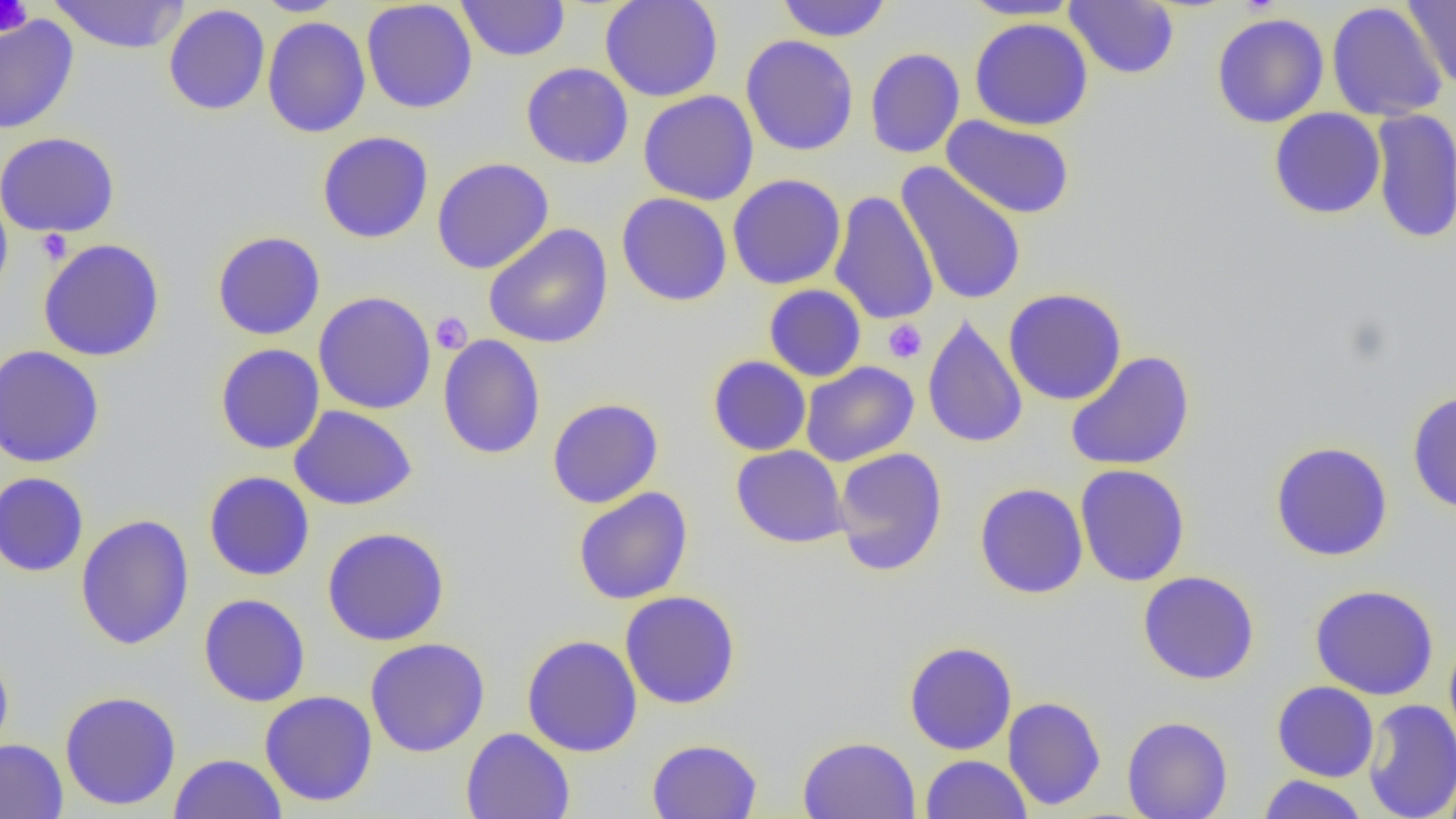

Summary:
  - Coordinate format: approximate bounding boxes as named x1/y1/x2/y2 corners in pixels
  - Uninfected red blood cell locations: (x1=48, y1=0, x2=190, y2=54), (x1=253, y1=0, x2=350, y2=16), (x1=361, y1=0, x2=478, y2=114), (x1=456, y1=0, x2=570, y2=62), (x1=599, y1=0, x2=724, y2=102), (x1=776, y1=0, x2=892, y2=42), (x1=961, y1=0, x2=1084, y2=20), (x1=1403, y1=0, x2=1456, y2=89), (x1=1065, y1=1, x2=1179, y2=79), (x1=1326, y1=2, x2=1448, y2=121), (x1=163, y1=4, x2=271, y2=116), (x1=1212, y1=12, x2=1329, y2=128), (x1=0, y1=15, x2=79, y2=135), (x1=261, y1=16, x2=371, y2=138), (x1=969, y1=17, x2=1094, y2=131), (x1=740, y1=34, x2=859, y2=156), (x1=865, y1=47, x2=965, y2=159), (x1=521, y1=62, x2=634, y2=169), (x1=638, y1=90, x2=759, y2=206), (x1=1268, y1=107, x2=1385, y2=219), (x1=1370, y1=109, x2=1456, y2=244), (x1=941, y1=115, x2=1075, y2=219), (x1=0, y1=131, x2=120, y2=238), (x1=317, y1=131, x2=434, y2=244), (x1=432, y1=157, x2=554, y2=274), (x1=896, y1=161, x2=1028, y2=305), (x1=727, y1=174, x2=846, y2=290), (x1=0, y1=186, x2=13, y2=303), (x1=829, y1=190, x2=939, y2=325), (x1=616, y1=192, x2=733, y2=306), (x1=484, y1=223, x2=613, y2=349), (x1=211, y1=231, x2=326, y2=340), (x1=38, y1=238, x2=165, y2=362), (x1=764, y1=284, x2=866, y2=382), (x1=1003, y1=288, x2=1127, y2=406), (x1=313, y1=291, x2=437, y2=414), (x1=922, y1=314, x2=1028, y2=449), (x1=437, y1=334, x2=546, y2=459), (x1=215, y1=343, x2=325, y2=455), (x1=0, y1=345, x2=105, y2=468), (x1=1064, y1=350, x2=1196, y2=471), (x1=707, y1=355, x2=811, y2=456), (x1=800, y1=361, x2=918, y2=466), (x1=1406, y1=389, x2=1456, y2=514), (x1=547, y1=397, x2=663, y2=508), (x1=289, y1=405, x2=418, y2=510), (x1=1269, y1=441, x2=1393, y2=561), (x1=731, y1=445, x2=848, y2=548), (x1=833, y1=447, x2=948, y2=576), (x1=1075, y1=464, x2=1190, y2=587), (x1=203, y1=471, x2=315, y2=581), (x1=0, y1=472, x2=89, y2=577), (x1=974, y1=482, x2=1088, y2=599), (x1=573, y1=487, x2=694, y2=605), (x1=75, y1=514, x2=195, y2=650), (x1=322, y1=526, x2=450, y2=646), (x1=1138, y1=571, x2=1260, y2=685), (x1=1309, y1=584, x2=1440, y2=701), (x1=620, y1=590, x2=741, y2=709), (x1=198, y1=593, x2=311, y2=707), (x1=1444, y1=633, x2=1456, y2=753), (x1=521, y1=634, x2=643, y2=757), (x1=365, y1=638, x2=490, y2=757), (x1=904, y1=641, x2=1017, y2=755), (x1=0, y1=648, x2=14, y2=763), (x1=1271, y1=680, x2=1379, y2=782), (x1=59, y1=690, x2=182, y2=810), (x1=260, y1=690, x2=378, y2=807), (x1=1003, y1=696, x2=1106, y2=810), (x1=1362, y1=698, x2=1456, y2=819), (x1=1122, y1=715, x2=1233, y2=819), (x1=460, y1=727, x2=575, y2=819), (x1=797, y1=735, x2=920, y2=818), (x1=0, y1=738, x2=68, y2=819), (x1=646, y1=738, x2=763, y2=819), (x1=169, y1=752, x2=287, y2=818), (x1=921, y1=754, x2=1032, y2=819), (x1=1441, y1=768, x2=1456, y2=818), (x1=1257, y1=774, x2=1369, y2=818)
  - Platelet locations: (x1=0, y1=0, x2=32, y2=36), (x1=36, y1=229, x2=71, y2=264), (x1=431, y1=311, x2=472, y2=355), (x1=883, y1=319, x2=927, y2=364)
  - Slide-level diagnosis: no evidence of blood parasites
  - Magnification: 1000x
  - Preparation: thin blood smear
  - Modality: optical microscopy
  - Field of view: single
  - Image size: 1456×819 pixels